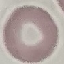
Summary:
  - Result: no malaria parasites detected
  - Preparation: thin smear
  - Stain: Giemsa
  - Capture: smartphone camera at the microscope eyepiece
  - Image type: cell patch, automatically extracted from a larger field of view and resized to 64 × 64 pixels